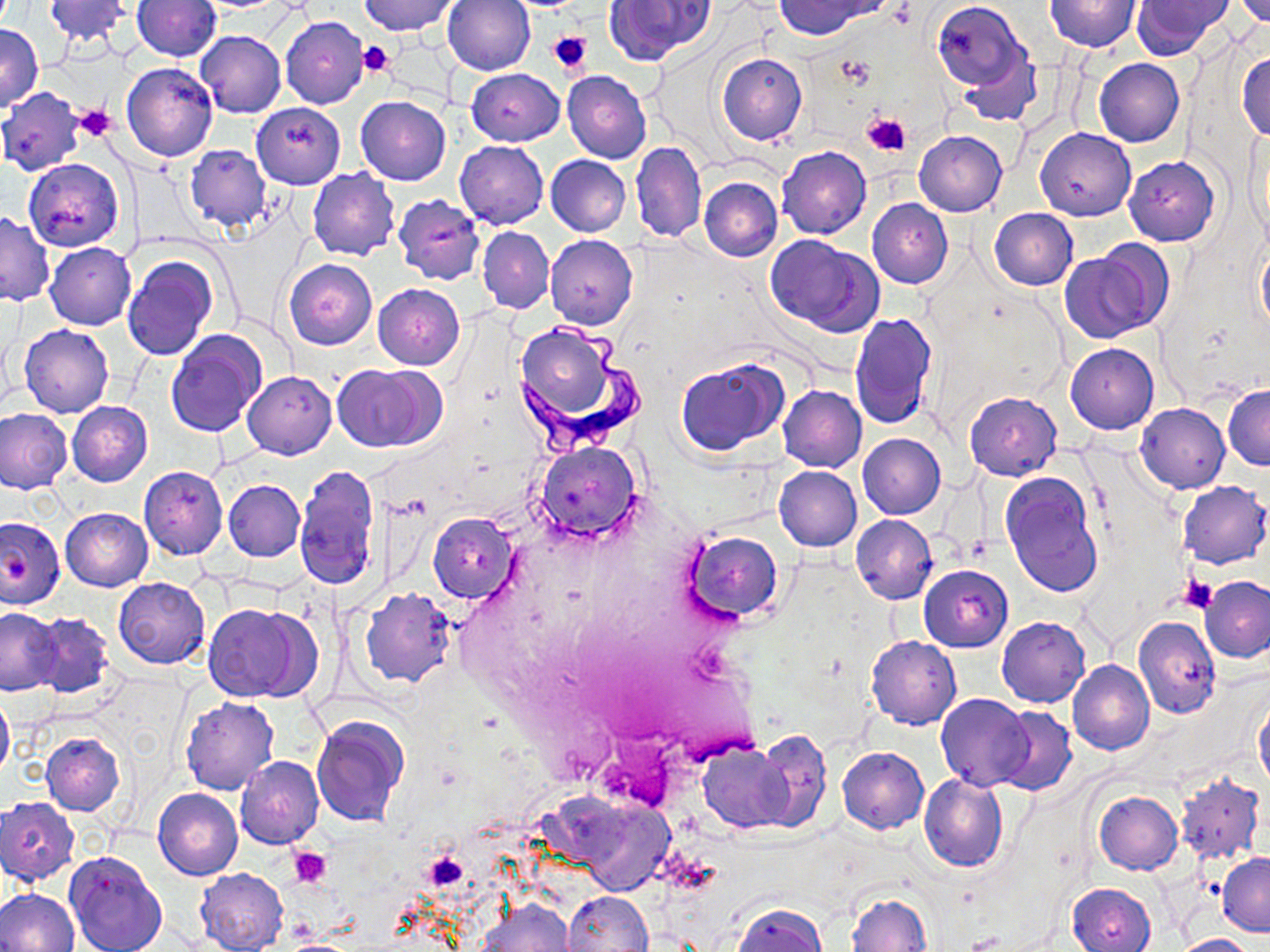 Approximate bounding boxes as (x1, y1, x2, y2) in pixels. Platelet locations: (547, 29, 593, 76), (358, 41, 395, 77), (835, 55, 876, 89), (74, 105, 119, 142), (862, 111, 912, 157), (7, 554, 36, 586), (1181, 577, 1217, 614), (289, 847, 332, 888), (422, 851, 468, 892). Uninfected red blood cell locations: (43, 0, 132, 47), (362, 0, 456, 35), (442, 0, 534, 76), (603, 0, 712, 66), (1045, 0, 1141, 52), (1232, 0, 1270, 25), (133, 1, 222, 61), (777, 1, 878, 38), (933, 1, 1027, 88), (1131, 1, 1229, 59), (281, 16, 368, 109), (0, 25, 42, 111), (196, 31, 286, 118), (956, 49, 1041, 128), (1236, 51, 1270, 142), (717, 52, 807, 146), (1094, 58, 1184, 147), (121, 62, 217, 162), (466, 69, 564, 145), (562, 71, 652, 163), (0, 87, 86, 175), (354, 95, 451, 185), (252, 103, 345, 188), (1036, 127, 1135, 221), (1245, 127, 1268, 240), (913, 130, 1007, 216), (456, 141, 548, 228), (631, 141, 706, 243), (184, 146, 272, 233), (776, 146, 871, 240), (545, 154, 631, 237), (1124, 156, 1220, 247), (23, 159, 124, 250), (698, 166, 873, 255), (307, 168, 401, 261), (700, 177, 782, 261), (393, 195, 484, 285), (867, 198, 953, 288), (989, 208, 1078, 291), (0, 211, 54, 307), (477, 227, 554, 314), (546, 234, 638, 331), (765, 235, 883, 337), (1256, 241, 1270, 334), (45, 242, 137, 329), (1064, 246, 1163, 341), (123, 256, 217, 360), (284, 259, 377, 350), (373, 283, 464, 370), (850, 311, 938, 430), (20, 324, 114, 418), (517, 326, 618, 423), (166, 329, 267, 439), (1065, 343, 1159, 433), (674, 356, 790, 457), (335, 365, 438, 452), (243, 371, 336, 459), (778, 385, 866, 472), (1223, 385, 1270, 469), (965, 392, 1060, 481), (67, 402, 153, 486), (1136, 403, 1230, 493), (0, 407, 73, 495), (857, 434, 946, 518), (532, 442, 643, 544), (295, 465, 381, 594), (138, 466, 227, 560), (774, 466, 862, 551), (1001, 471, 1104, 598), (224, 479, 305, 561), (1177, 480, 1270, 569), (61, 508, 152, 591), (0, 514, 65, 609), (428, 514, 517, 603), (851, 515, 937, 604), (683, 531, 783, 624), (920, 565, 1012, 652), (1200, 575, 1270, 663), (113, 577, 209, 669), (1164, 585, 1259, 692), (360, 588, 456, 688), (205, 604, 309, 702), (0, 607, 63, 695), (28, 612, 115, 700), (997, 616, 1090, 708), (1133, 617, 1220, 717), (867, 635, 961, 729), (1068, 660, 1154, 756), (0, 691, 13, 782), (936, 694, 1033, 790), (181, 697, 278, 795), (1254, 701, 1270, 789), (994, 704, 1077, 796), (312, 716, 407, 827), (752, 729, 831, 834), (42, 733, 125, 815), (698, 743, 797, 833), (837, 746, 928, 834), (236, 756, 324, 848), (1172, 772, 1265, 866), (919, 774, 1008, 872), (153, 787, 242, 880), (1094, 791, 1183, 875), (559, 792, 678, 896), (1, 797, 79, 886), (64, 850, 166, 952), (1216, 852, 1270, 936), (194, 868, 289, 951), (1067, 882, 1157, 952), (0, 888, 79, 952), (564, 890, 653, 952), (846, 892, 931, 951), (477, 899, 575, 952), (732, 904, 828, 952), (1171, 934, 1257, 952). Trypanosoma brucei locations: (508, 324, 648, 454). Slide-level diagnosis: Trypanosoma brucei. Light microscopy. Thin blood film. Single field of view. Captured at 1000x magnification. Image is 1270×952 pixels. May-Grünwald-Giemsa-stained preparation.